Classify this cell by malaria status.
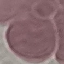
It is uninfected.

Summary:
  - Preparation: thin smear
  - Image type: automatically extracted cell patch, resized to 64 × 64 pixels
  - Capture: smartphone camera at the microscope eyepiece
  - Stain: Giemsa